Give the position of every malaria parasite.
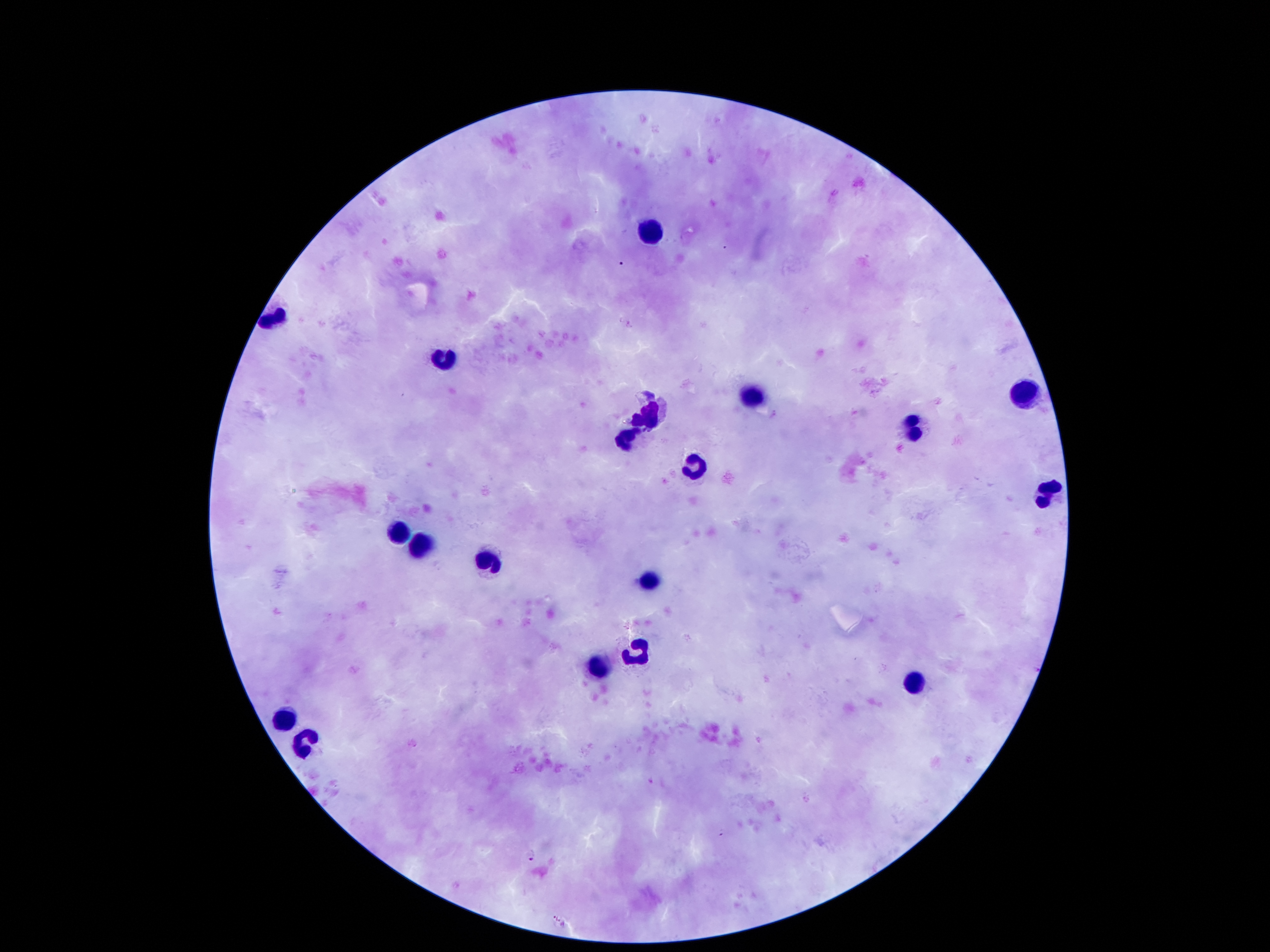
Approximate centers as {x, y} in pixels.
Malaria parasites: {726, 247}, {622, 263}, {630, 324}, {721, 832}, {532, 854}, {556, 917}.

Leukocyte locations: {650, 234}, {445, 358}, {1020, 395}, {756, 398}, {650, 412}, {912, 432}, {623, 436}, {697, 468}, {1052, 488}, {400, 528}, {422, 545}, {492, 565}, {647, 578}, {635, 649}, {590, 667}, {912, 683}, {286, 724}, {305, 746}. Image is 1270×952 pixels. 100x magnification. Thick blood smear. Smartphone photograph taken through the microscope eyepiece. Patient malaria status: infected with Plasmodium falciparum. Single field of view. Giemsa stain.